Locate and identify every blood parasite.
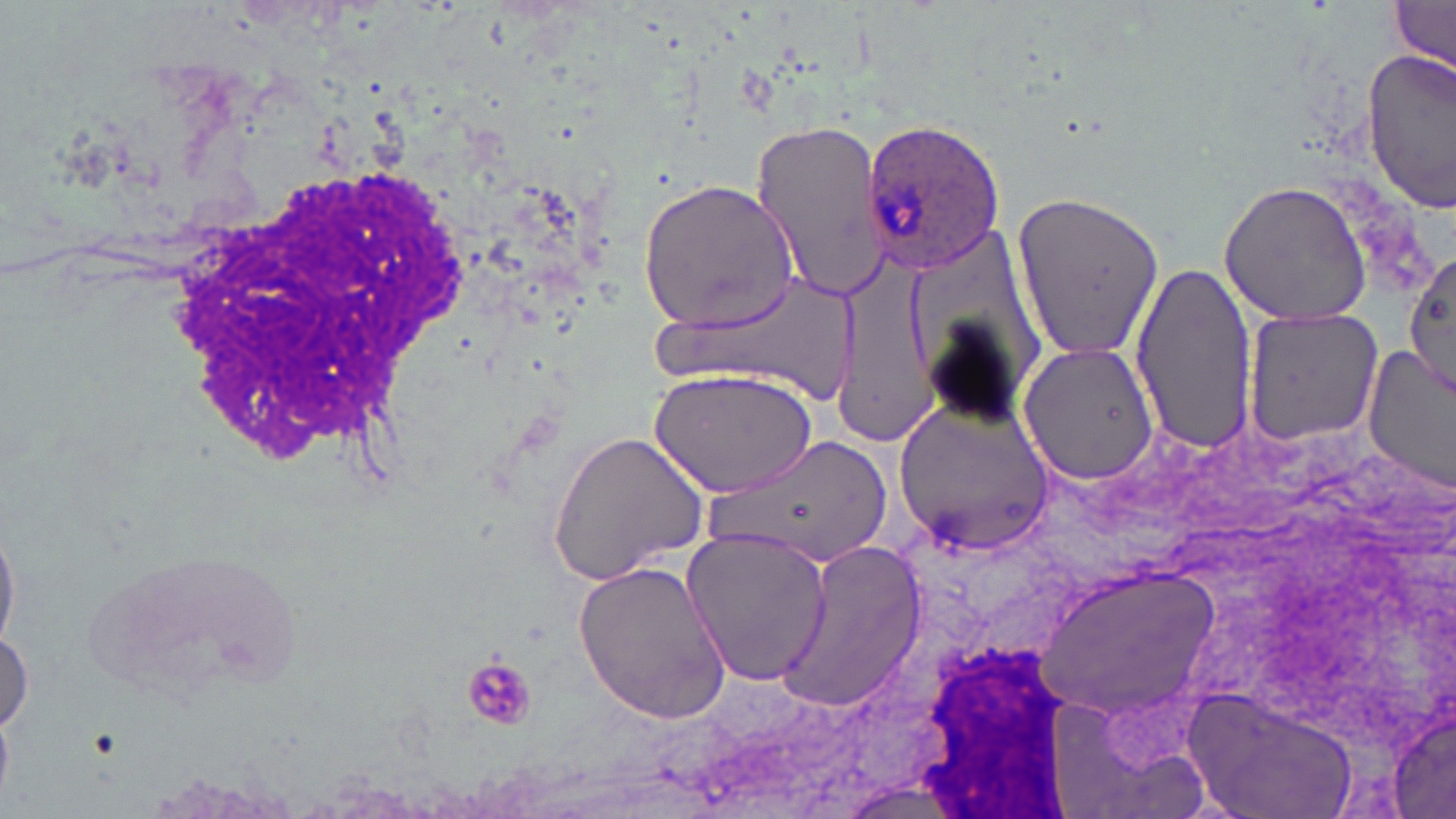
Approximate bounding boxes as (x1, y1, x2, y2) in pixels.
Plasmodium ovale-infected red blood cells: (860, 115, 1010, 273).
No Plasmodium falciparum, Plasmodium malariae, Plasmodium vivax, Babesia divergens, or Trypanosoma brucei observed.

White blood cell locations: (161, 162, 476, 473). Platelet locations: (462, 658, 538, 730). Uninfected red blood cell locations: (1389, 2, 1456, 71), (1362, 50, 1455, 213), (751, 117, 889, 303), (637, 178, 800, 333), (1217, 180, 1373, 328), (1008, 185, 1165, 363), (1404, 248, 1454, 399), (1131, 260, 1258, 454), (651, 272, 863, 400), (1244, 308, 1385, 447), (1018, 343, 1157, 487), (1362, 348, 1456, 493), (655, 365, 816, 499), (892, 394, 1060, 552), (545, 427, 712, 589), (710, 432, 892, 572), (0, 518, 19, 655), (679, 526, 833, 687), (772, 544, 925, 715), (572, 558, 733, 724), (1033, 560, 1220, 722), (1187, 685, 1360, 819), (1386, 707, 1456, 818). Slide-level diagnosis: Plasmodium ovale. Light microscopy. May-Grünwald-Giemsa-stained preparation. Thin blood film. Captured at 1000x magnification. Single field of view. Image is 1456×819 pixels.